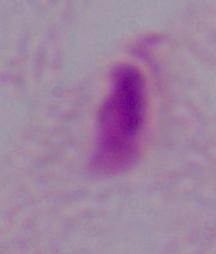
magnification = 1000x
identification = trichomonad
modality = micrograph